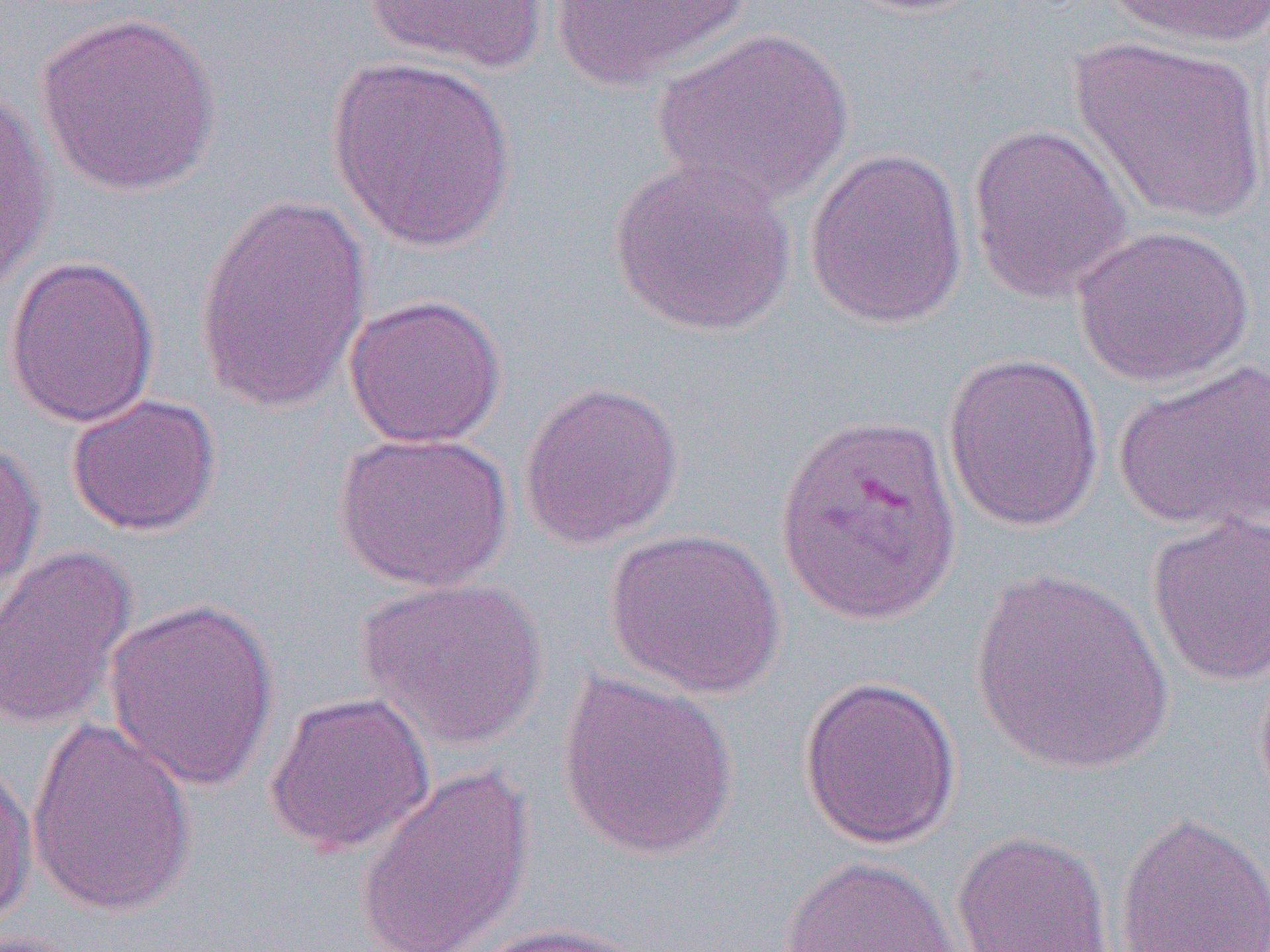

Summary:
  - Coordinate format: approximate bounding boxes as named x1/y1/x2/y2 corners in pixels
  - Uninfected red blood cell locations: (x1=364, y1=0, x2=550, y2=74), (x1=550, y1=0, x2=751, y2=91), (x1=1100, y1=0, x2=1270, y2=48), (x1=33, y1=10, x2=223, y2=197), (x1=652, y1=27, x2=854, y2=206), (x1=1069, y1=35, x2=1267, y2=225), (x1=325, y1=54, x2=518, y2=252), (x1=0, y1=83, x2=56, y2=294), (x1=966, y1=122, x2=1134, y2=304), (x1=803, y1=147, x2=969, y2=330), (x1=607, y1=157, x2=797, y2=337), (x1=192, y1=192, x2=372, y2=414), (x1=1072, y1=223, x2=1255, y2=389), (x1=2, y1=255, x2=160, y2=429), (x1=343, y1=293, x2=507, y2=449), (x1=941, y1=351, x2=1104, y2=533), (x1=1113, y1=361, x2=1270, y2=534), (x1=517, y1=380, x2=684, y2=551), (x1=66, y1=392, x2=222, y2=537), (x1=333, y1=431, x2=514, y2=592), (x1=0, y1=439, x2=46, y2=601), (x1=1146, y1=513, x2=1270, y2=686), (x1=603, y1=527, x2=785, y2=700), (x1=0, y1=544, x2=138, y2=732), (x1=968, y1=566, x2=1176, y2=779), (x1=356, y1=577, x2=548, y2=751), (x1=102, y1=596, x2=279, y2=792), (x1=555, y1=670, x2=739, y2=862), (x1=797, y1=675, x2=963, y2=850), (x1=263, y1=690, x2=436, y2=856), (x1=26, y1=717, x2=196, y2=917), (x1=0, y1=753, x2=38, y2=927), (x1=354, y1=764, x2=537, y2=951), (x1=1113, y1=809, x2=1270, y2=952), (x1=950, y1=829, x2=1115, y2=951), (x1=777, y1=854, x2=962, y2=952), (x1=461, y1=921, x2=650, y2=952)
  - Plasmodium vivax-infected red blood cell locations: (x1=774, y1=412, x2=964, y2=627)
  - Slide-level diagnosis: Plasmodium vivax
  - Modality: light microscopy
  - Image size: 1270×952 pixels
  - Preparation: thin blood film
  - Magnification: 1000x
  - Field of view: single